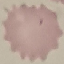

Summary:
  - Malaria status: uninfected
  - Image type: cell patch, automatically extracted from a larger field of view and resized to 64 × 64 pixels
  - Preparation: thin smear
  - Stain: Giemsa
  - Capture: smartphone camera at the microscope eyepiece